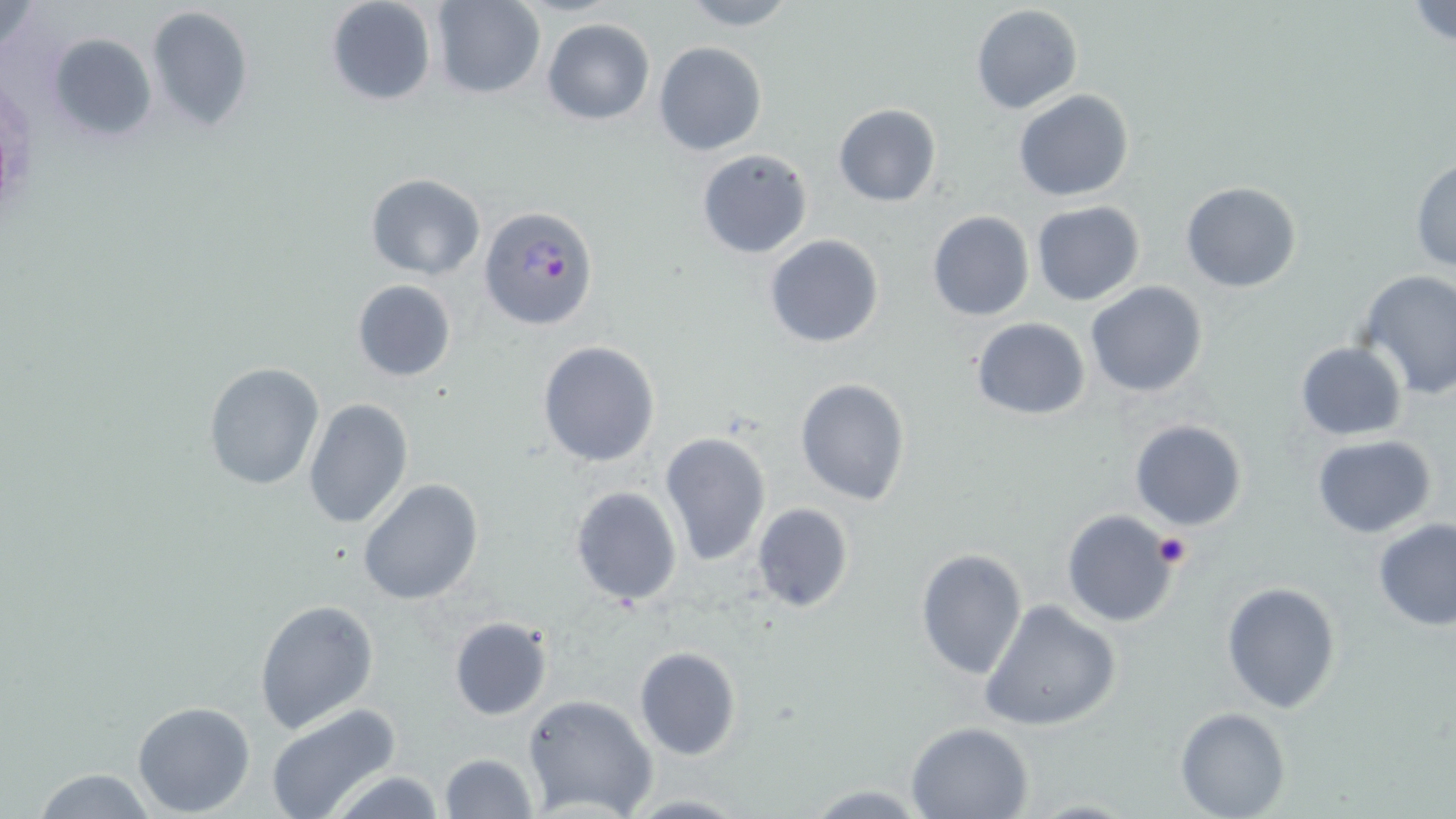

Approximate bounding boxes as (x1,y1)-(x2,y2) corner pairs in pixels. Plasmodium falciparum-infected red blood cell locations: (480,205)-(600,332). Platelet locations: (1152,532)-(1192,569). Uninfected red blood cell locations: (0,0)-(47,55), (325,0)-(438,107), (675,0)-(801,31), (1406,0)-(1456,51), (430,1)-(545,98), (146,4)-(254,135), (970,4)-(1084,114), (540,18)-(655,124), (48,33)-(157,143), (654,40)-(767,157), (1013,90)-(1135,202), (833,103)-(941,206), (696,148)-(815,260), (1410,156)-(1456,271), (366,173)-(485,279), (1180,181)-(1302,293), (1031,201)-(1145,306), (928,210)-(1034,322), (764,234)-(885,348), (1353,269)-(1456,399), (352,279)-(457,381), (1085,280)-(1209,398), (971,317)-(1090,420), (537,340)-(662,468), (1295,341)-(1407,441), (1302,345)-(1418,536), (203,362)-(324,490), (794,379)-(911,505), (303,398)-(413,527), (1128,418)-(1249,531), (659,431)-(771,567), (1312,435)-(1437,538), (358,478)-(485,606), (569,485)-(683,607), (750,503)-(855,614), (1061,510)-(1180,626), (1372,518)-(1456,632), (915,549)-(1028,681), (1221,581)-(1342,715), (254,598)-(380,735), (979,599)-(1121,734), (448,615)-(554,722), (633,647)-(743,761), (521,693)-(658,818), (131,701)-(256,816), (265,704)-(405,819), (1175,707)-(1290,819), (904,721)-(1034,819), (438,752)-(540,819), (25,765)-(163,819), (323,771)-(447,818), (801,783)-(930,816), (616,794)-(754,817). Slide-level diagnosis: Plasmodium falciparum. Image is 1456×819 pixels. Light microscopy. Thin blood film. 1000x magnification. Single field of view. May-Grünwald-Giemsa stain.